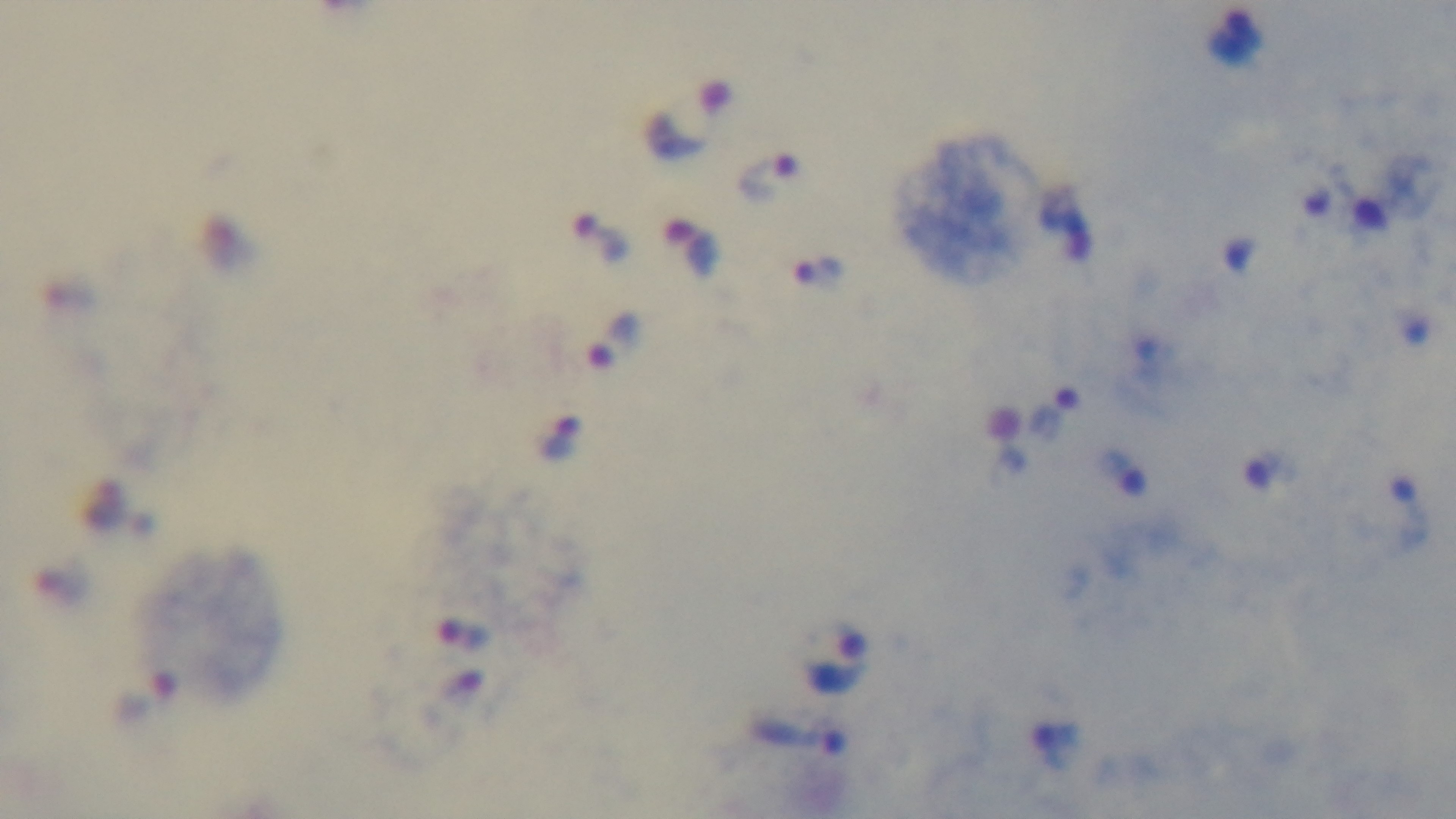
Summary:
  - Stain: Giemsa
  - Modality: light microscopy
  - Capture: mounted 4K digital camera
  - Objective: 100x oil immersion
  - Field of view: single
  - Malaria status: infected
  - Preparation: thick